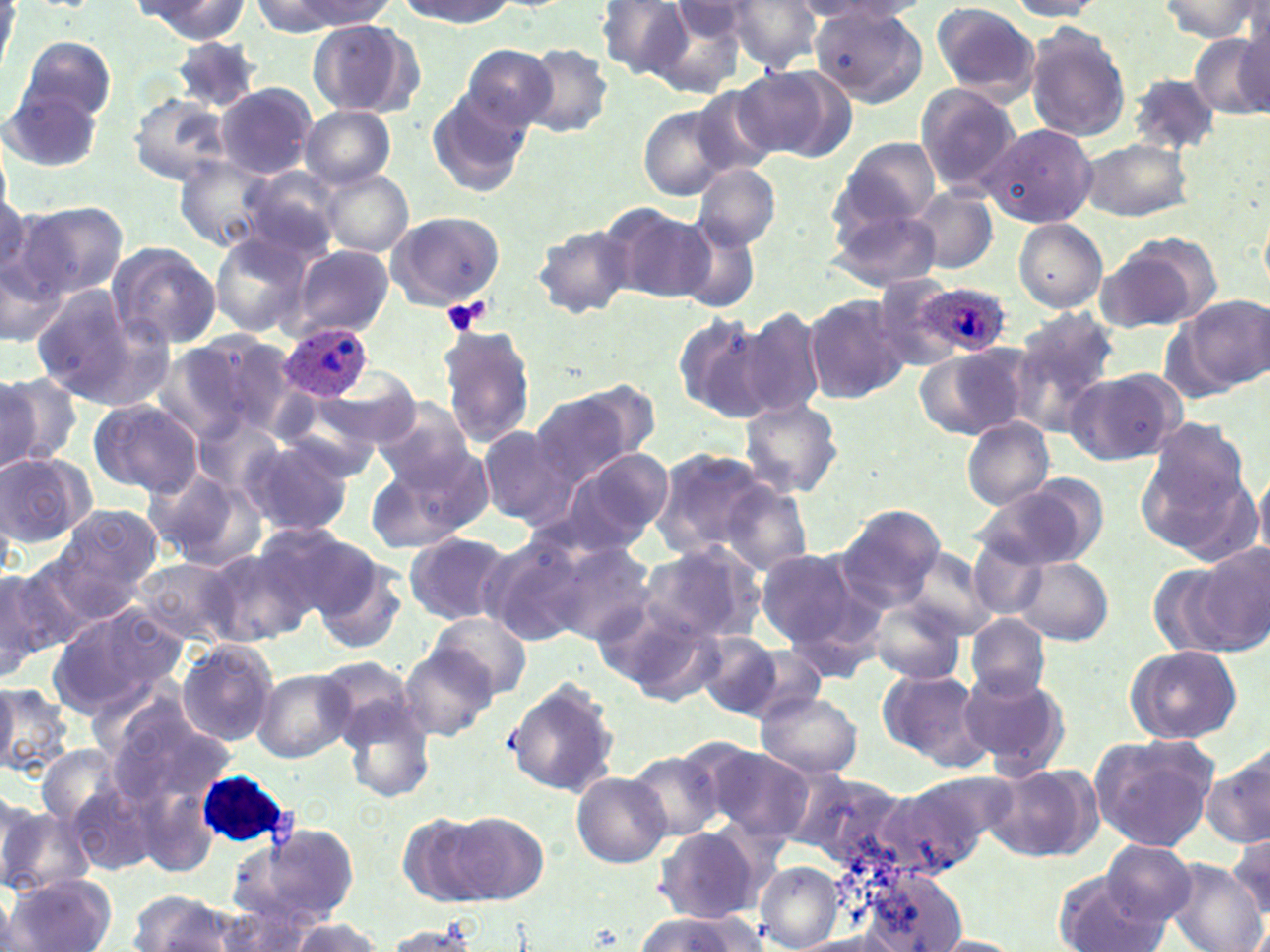
Approximate bounding boxes as (x1, y1, x2, y2) in pixels. Uninfected red blood cell locations: (395, 0, 517, 28), (725, 0, 822, 72), (0, 1, 16, 79), (133, 1, 249, 42), (249, 1, 373, 35), (599, 1, 691, 79), (809, 1, 926, 23), (1006, 1, 1106, 20), (1157, 1, 1265, 43), (664, 3, 760, 55), (807, 3, 928, 106), (930, 3, 1042, 102), (645, 4, 747, 100), (307, 19, 421, 118), (1024, 21, 1133, 142), (1190, 28, 1270, 121), (16, 36, 115, 124), (174, 39, 261, 114), (461, 43, 559, 131), (518, 45, 615, 138), (741, 64, 856, 163), (1129, 72, 1222, 155), (686, 82, 784, 179), (7, 83, 105, 172), (215, 83, 317, 178), (915, 84, 1022, 196), (425, 85, 536, 198), (128, 93, 230, 187), (300, 105, 395, 189), (639, 105, 730, 198), (980, 123, 1097, 229), (1075, 134, 1192, 224), (837, 136, 941, 227), (175, 156, 275, 253), (693, 164, 780, 250), (239, 166, 346, 260), (317, 168, 413, 256), (0, 181, 33, 292), (909, 187, 1000, 273), (824, 201, 941, 292), (17, 202, 129, 301), (601, 203, 714, 302), (384, 211, 507, 313), (670, 218, 764, 312), (1014, 218, 1107, 312), (531, 223, 638, 319), (210, 232, 314, 338), (1099, 237, 1215, 332), (107, 243, 223, 350), (0, 244, 69, 350), (291, 246, 393, 339), (866, 276, 968, 370), (30, 284, 143, 400), (803, 294, 908, 404), (1175, 296, 1269, 394), (736, 306, 828, 421), (1011, 310, 1118, 423), (673, 314, 774, 426), (436, 322, 535, 446), (180, 330, 301, 440), (915, 347, 1030, 441), (1066, 369, 1183, 466), (318, 370, 423, 451), (0, 372, 72, 474), (528, 384, 649, 484), (87, 397, 203, 498), (738, 397, 845, 500), (370, 398, 476, 489), (1140, 415, 1260, 558), (962, 418, 1052, 510), (476, 426, 575, 527), (237, 435, 357, 540), (557, 445, 675, 551), (651, 448, 776, 558), (365, 450, 487, 553), (0, 452, 94, 546), (146, 468, 263, 573), (1252, 470, 1270, 564), (974, 479, 1103, 571), (719, 482, 814, 574), (833, 503, 946, 612), (51, 505, 162, 608), (250, 521, 369, 621), (402, 531, 517, 627), (477, 533, 596, 647), (967, 537, 1052, 619), (543, 539, 658, 646), (637, 540, 769, 648), (1195, 544, 1270, 655), (754, 547, 868, 648), (201, 550, 306, 648), (311, 553, 407, 655), (133, 557, 239, 644), (1014, 558, 1114, 646), (4, 560, 100, 661), (0, 567, 56, 676), (599, 597, 726, 704), (868, 598, 966, 685), (47, 604, 183, 714), (429, 610, 531, 701), (965, 613, 1051, 702), (694, 629, 785, 719), (177, 640, 280, 746), (727, 641, 830, 723), (399, 644, 497, 742), (1123, 644, 1242, 745), (876, 668, 987, 771), (252, 669, 355, 762), (958, 669, 1070, 776), (505, 676, 619, 797), (0, 685, 73, 778), (757, 691, 862, 778), (342, 697, 435, 803), (107, 703, 231, 809), (1089, 733, 1219, 850), (698, 743, 816, 843), (1202, 746, 1270, 849), (628, 748, 727, 841), (983, 761, 1099, 863), (787, 770, 910, 871), (572, 771, 671, 867), (884, 777, 1000, 878), (66, 779, 156, 879), (0, 802, 87, 897), (396, 810, 505, 906), (446, 810, 549, 903), (230, 822, 362, 930), (654, 826, 763, 924), (1227, 827, 1270, 923), (1099, 841, 1198, 926), (1165, 859, 1266, 952), (755, 863, 842, 951), (850, 865, 971, 951), (1052, 871, 1170, 952), (5, 873, 117, 952), (128, 891, 238, 952), (205, 904, 315, 952), (633, 912, 770, 952), (282, 917, 386, 951), (381, 922, 482, 952), (785, 934, 912, 951), (927, 934, 1028, 951). Platelet locations: (440, 296, 489, 338). Plasmodium ovale-infected red blood cell locations: (908, 282, 1010, 360), (281, 324, 374, 400), (197, 770, 293, 847). Slide-level diagnosis: Plasmodium ovale. Light microscopy. 1000x magnification. Thin blood film. Image is 1270×952 pixels. May-Grünwald-Giemsa-stained preparation. Single field of view.